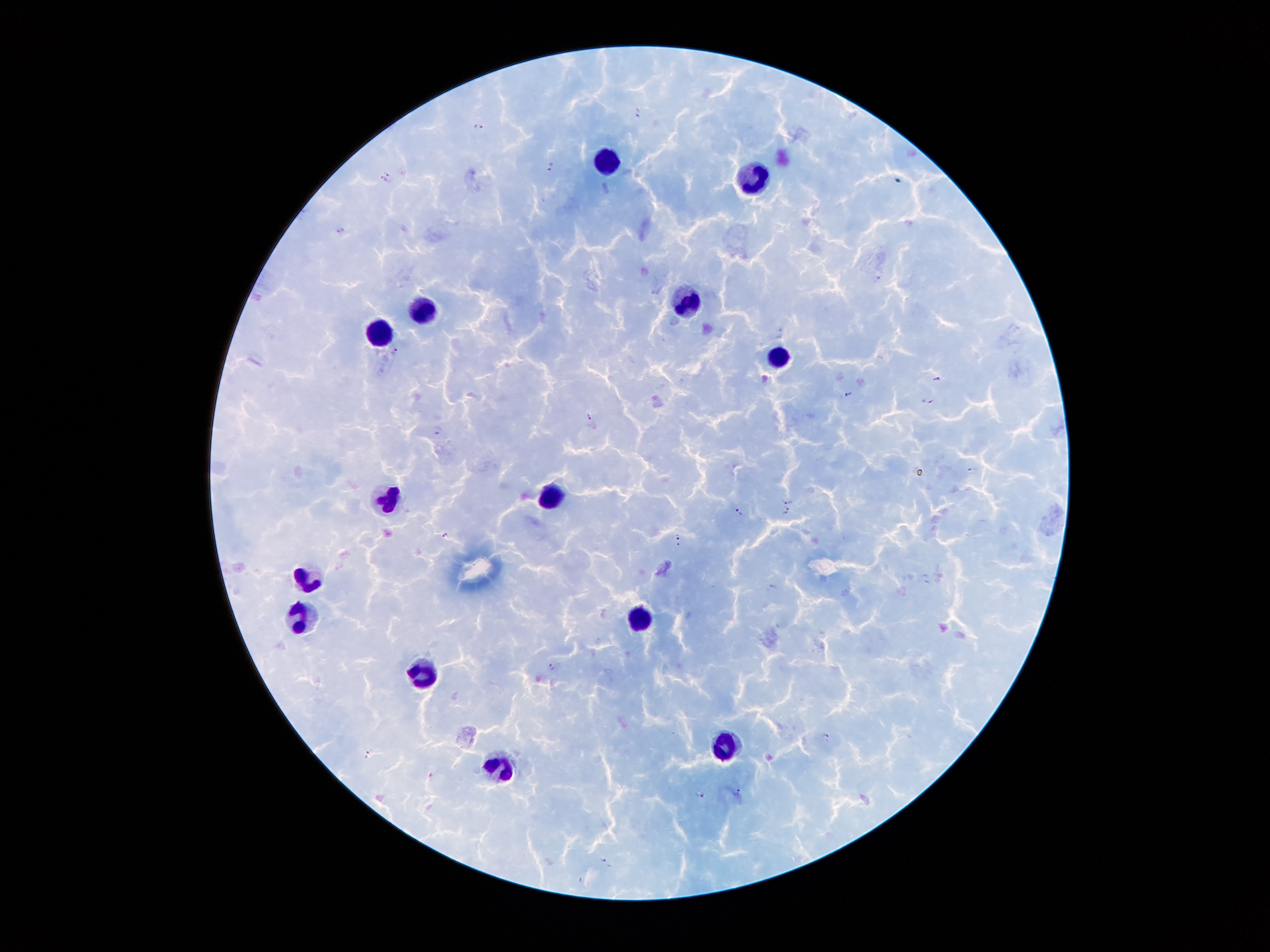
Approximate centers as (x, y) in pixels. Leukocyte locations: (604, 161), (757, 182), (689, 302), (427, 313), (381, 332), (777, 357), (552, 496), (391, 500), (307, 580), (302, 620), (640, 621), (425, 677), (726, 745), (500, 769). Malaria parasite locations: (636, 112), (480, 124), (551, 165), (385, 176), (340, 229), (880, 275), (778, 333), (395, 352), (938, 378), (847, 393), (928, 400), (589, 414), (438, 431), (972, 470), (787, 500), (737, 512), (786, 512), (446, 535), (680, 539), (925, 579), (774, 587), (552, 667), (826, 737), (369, 754), (738, 791), (701, 793), (606, 861). Thick blood smear. Single field of view. Patient malaria status: infected with Plasmodium falciparum. Smartphone photograph taken through the microscope eyepiece. Image is 1270×952 pixels. 100x magnification. Giemsa stain.